Point out each Plasmodium parasite.
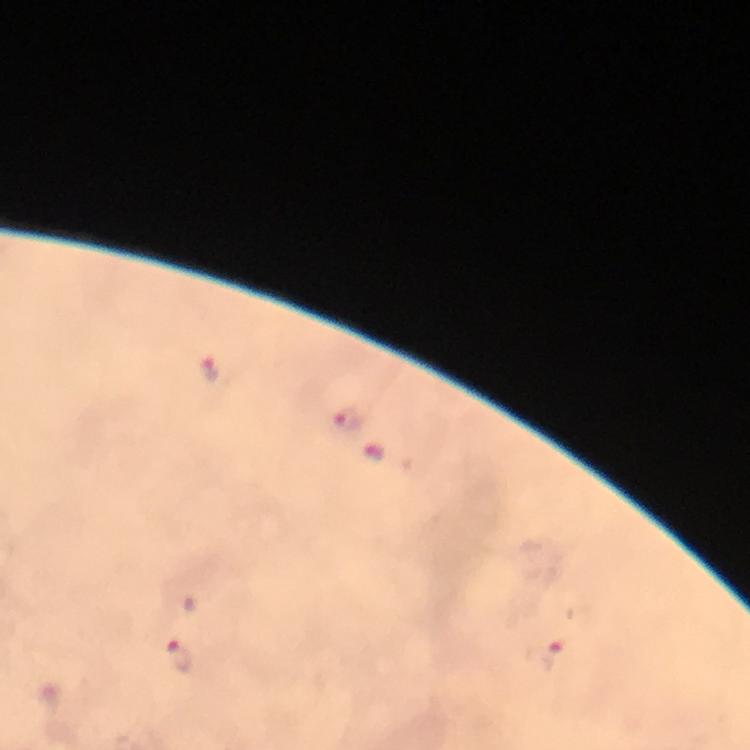

Approximate centers as {x, y} in pixels.
Plasmodium parasites: {211, 370}, {345, 420}, {377, 452}, {548, 655}, {177, 657}.

Immersion oil was used. A crop from one field of view. Giemsa-stained preparation. Thick blood smear. Image is 750×750 pixels. From a malaria diagnostic workup. At 100x magnification. Smartphone photograph taken through a microscope.